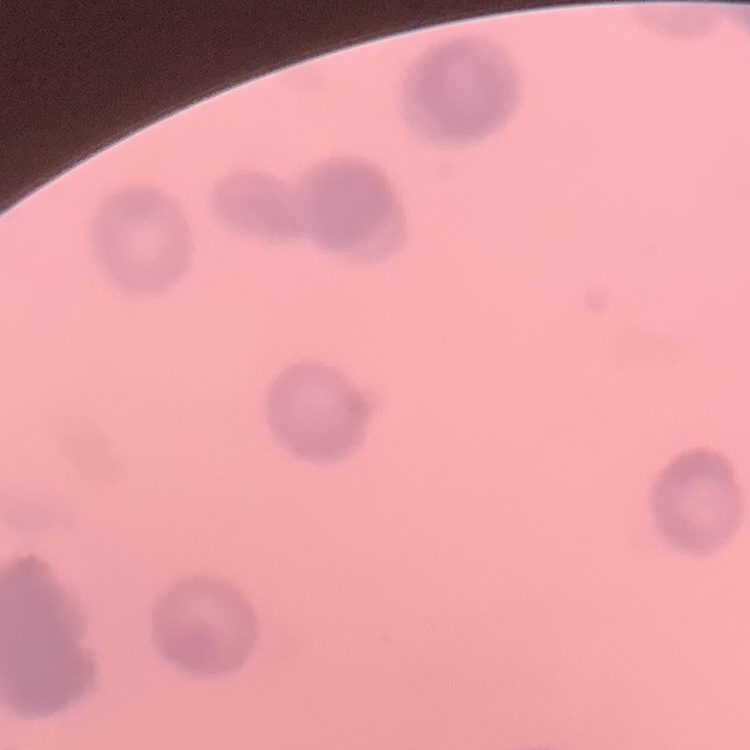

The red blood cells exhibit rouleaux formation. Thin blood film. Square crop of a larger photomicrograph. Stained with either Field's or Giemsa.